Give the extent of all white blood cells.
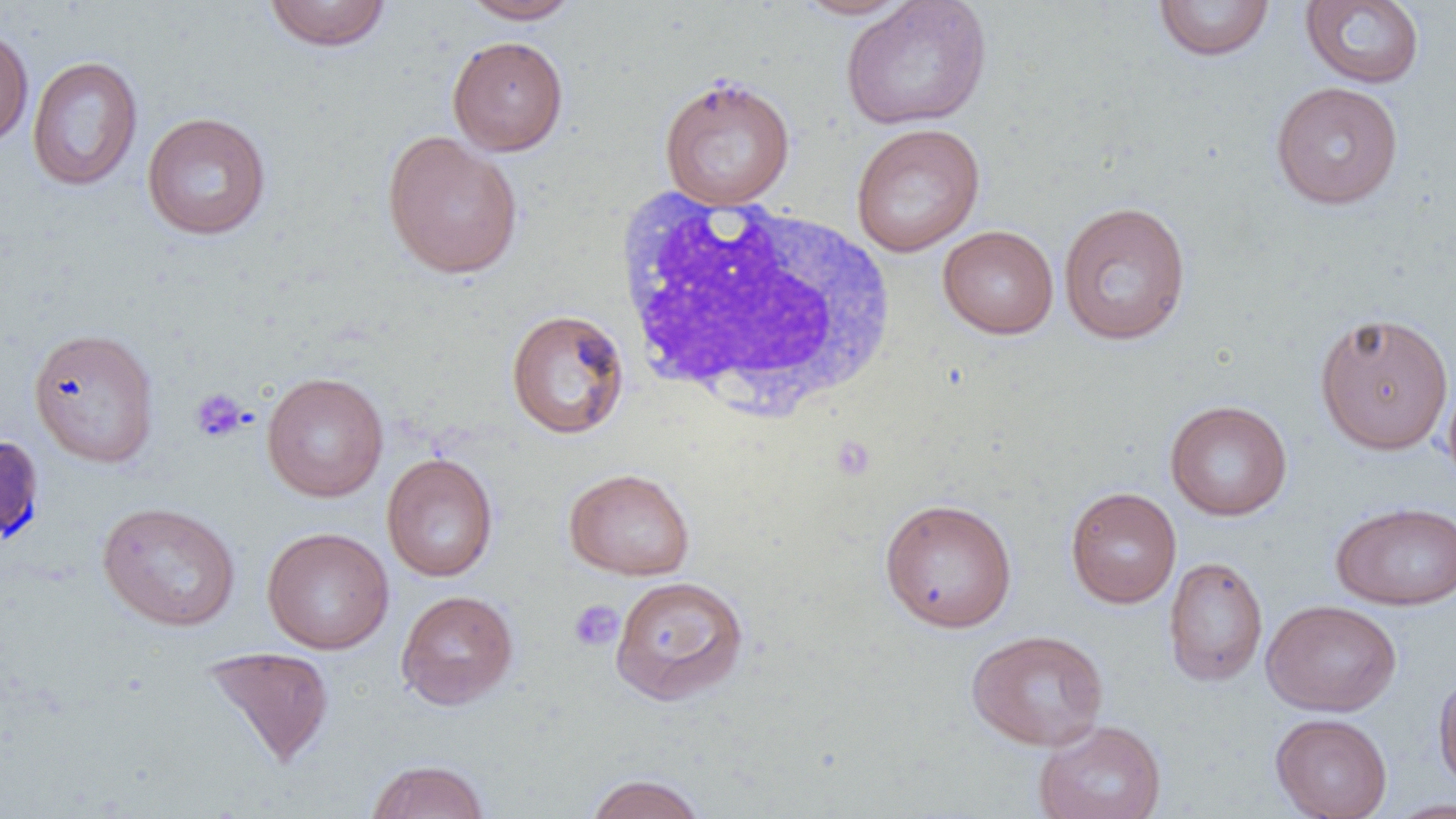
Approximate bounding boxes as [x1, y1, x2, y2] in pixels.
White blood cells: [611, 189, 898, 422].

slide-level diagnosis = negative for blood parasites
field of view = one of a larger specimen
platelet locations = approximate bounding boxes as [x1, y1, x2, y2] in pixels: [190, 388, 249, 443], [831, 435, 876, 480], [569, 599, 624, 653]
image size = 1456×819 pixels
magnification = 1000x
uninfected red blood cell locations = approximate bounding boxes as [x1, y1, x2, y2] in pixels: [791, 0, 917, 20], [840, 0, 992, 130], [263, 1, 392, 51], [459, 1, 583, 24], [1152, 1, 1276, 61], [1300, 1, 1425, 89], [0, 24, 34, 150], [447, 35, 568, 156], [26, 55, 143, 191], [658, 75, 796, 210], [1270, 81, 1404, 209], [141, 111, 272, 240], [850, 122, 986, 257], [382, 129, 524, 279], [1058, 201, 1192, 345], [937, 225, 1059, 339], [505, 308, 630, 439], [1313, 312, 1454, 456], [27, 326, 161, 468], [1441, 368, 1456, 495], [261, 371, 389, 502], [1164, 399, 1292, 521], [382, 453, 498, 582], [563, 467, 696, 581], [1065, 486, 1181, 609], [879, 497, 1018, 633], [97, 500, 241, 631], [1330, 500, 1456, 611], [262, 526, 394, 655], [1163, 555, 1268, 687], [609, 575, 749, 705], [395, 589, 519, 710], [1262, 598, 1402, 717], [966, 629, 1109, 751], [201, 645, 335, 768], [1434, 670, 1456, 794], [1270, 712, 1393, 818], [1033, 719, 1166, 819], [364, 759, 490, 819], [584, 773, 707, 819], [1383, 798, 1456, 819]
preparation = thin blood film
modality = light microscopy